Classify this cell by malaria status.
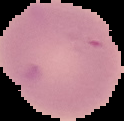

It is uninfected.

Image is 124×121 pixels. The area outside the segmented cell region is set to black. From a thin blood smear.